Draw a bounding box around every artifact (platelet-like body, stain precipitate, or debris).
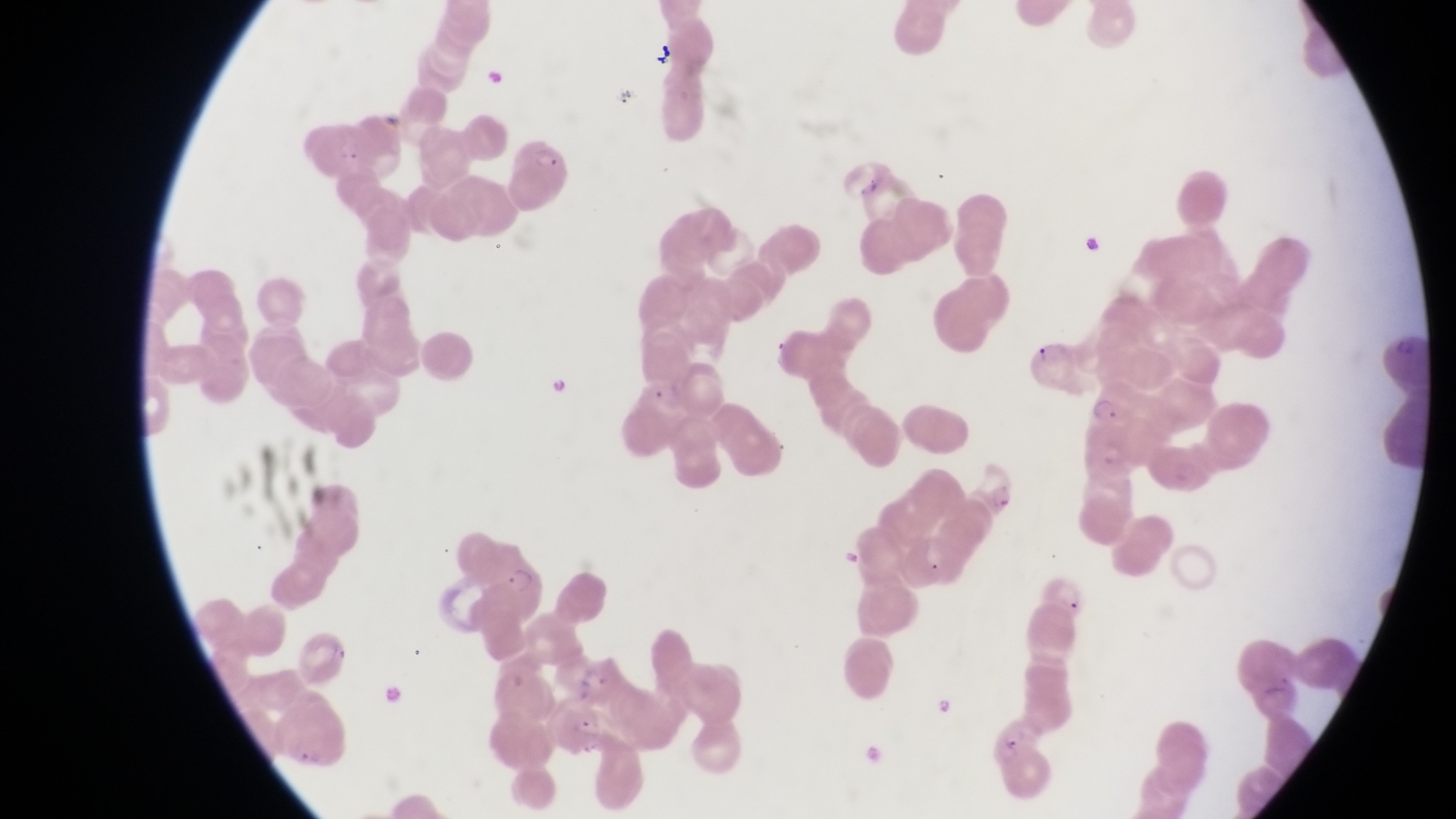

Approximate bounding boxes as [left, top, right, bottom] in pixels.
Artifacts (platelet-like body, stain precipitate, or debris): [1081, 224, 1111, 266], [325, 640, 355, 663].

Trophozoite locations: [544, 370, 583, 397], [1083, 389, 1128, 428], [934, 690, 955, 719]. Parasitised red blood cell locations: [510, 140, 577, 207], [1027, 338, 1090, 397], [453, 535, 543, 618], [1039, 576, 1094, 621], [987, 717, 1046, 770]. Captured by a smartphone held over the eyepiece of an Olympus CX-23 microscope. At a magnification of 1000x. Image is 1456×819 pixels. Sample from Uganda. Thin blood film. Single field of view.